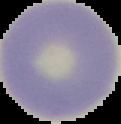

image type = segmented cell region with the area outside set to black
preparation = thin blood smear
result = negative for Plasmodium parasites
image size = 121×124 pixels